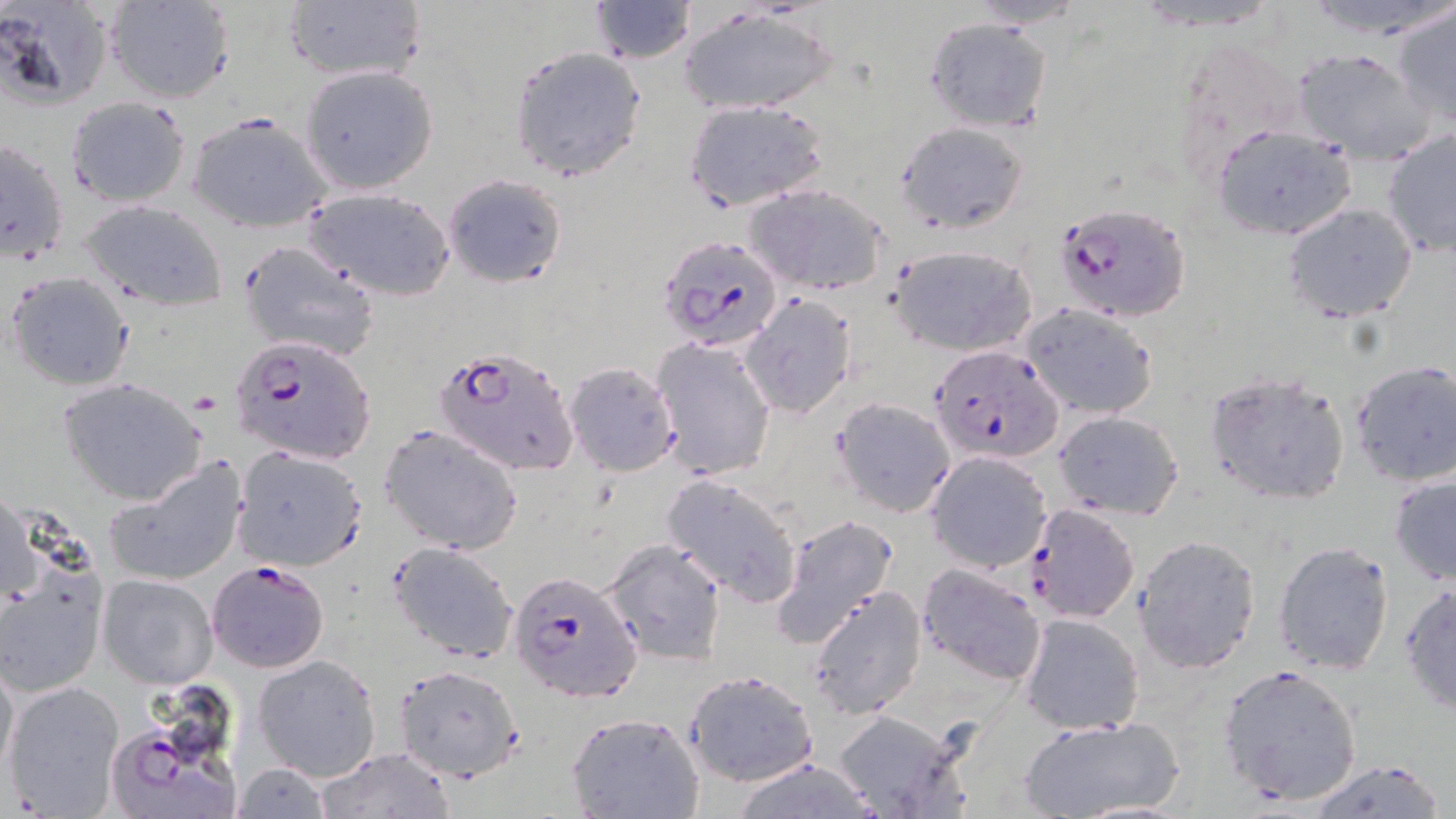
Approximate bounding boxes as named x1/y1/x2/y2 corners in pixels. Platelet locations: (x1=190, y1=391, x2=221, y2=416). Plasmodium falciparum-infected red blood cell locations: (x1=1053, y1=201, x2=1191, y2=322), (x1=656, y1=233, x2=786, y2=351), (x1=232, y1=335, x2=376, y2=463), (x1=431, y1=344, x2=578, y2=478), (x1=931, y1=344, x2=1064, y2=463), (x1=1025, y1=503, x2=1140, y2=623), (x1=206, y1=560, x2=329, y2=674), (x1=507, y1=570, x2=644, y2=701), (x1=110, y1=716, x2=247, y2=819). Uninfected red blood cell locations: (x1=1, y1=0, x2=115, y2=111), (x1=104, y1=0, x2=235, y2=104), (x1=283, y1=0, x2=429, y2=85), (x1=970, y1=0, x2=1087, y2=28), (x1=1298, y1=0, x2=1455, y2=36), (x1=588, y1=1, x2=697, y2=63), (x1=1390, y1=3, x2=1455, y2=130), (x1=679, y1=9, x2=838, y2=115), (x1=923, y1=16, x2=1052, y2=134), (x1=508, y1=44, x2=649, y2=182), (x1=1290, y1=47, x2=1435, y2=162), (x1=300, y1=65, x2=439, y2=195), (x1=65, y1=97, x2=191, y2=206), (x1=683, y1=99, x2=831, y2=213), (x1=189, y1=114, x2=329, y2=233), (x1=895, y1=121, x2=1029, y2=235), (x1=1210, y1=123, x2=1358, y2=241), (x1=1382, y1=132, x2=1455, y2=257), (x1=0, y1=137, x2=70, y2=264), (x1=441, y1=174, x2=568, y2=287), (x1=743, y1=183, x2=891, y2=297), (x1=304, y1=188, x2=456, y2=301), (x1=81, y1=199, x2=227, y2=310), (x1=1282, y1=202, x2=1418, y2=323), (x1=237, y1=240, x2=379, y2=362), (x1=885, y1=244, x2=1038, y2=355), (x1=5, y1=271, x2=133, y2=391), (x1=740, y1=295, x2=857, y2=419), (x1=1020, y1=301, x2=1161, y2=419), (x1=651, y1=337, x2=777, y2=480), (x1=1349, y1=358, x2=1456, y2=487), (x1=562, y1=361, x2=681, y2=476), (x1=1204, y1=371, x2=1352, y2=505), (x1=59, y1=377, x2=207, y2=506), (x1=831, y1=397, x2=956, y2=518), (x1=1051, y1=410, x2=1184, y2=521), (x1=378, y1=423, x2=524, y2=556), (x1=232, y1=444, x2=368, y2=572), (x1=925, y1=451, x2=1052, y2=573), (x1=102, y1=458, x2=248, y2=587), (x1=1388, y1=472, x2=1456, y2=587), (x1=661, y1=474, x2=802, y2=607), (x1=1, y1=491, x2=38, y2=608), (x1=769, y1=515, x2=899, y2=650), (x1=1131, y1=534, x2=1262, y2=673), (x1=601, y1=537, x2=727, y2=667), (x1=387, y1=540, x2=519, y2=664), (x1=1272, y1=543, x2=1396, y2=675), (x1=0, y1=557, x2=107, y2=698), (x1=915, y1=561, x2=1047, y2=686), (x1=97, y1=573, x2=220, y2=691), (x1=1398, y1=583, x2=1455, y2=713), (x1=806, y1=585, x2=927, y2=719), (x1=1018, y1=612, x2=1145, y2=735), (x1=252, y1=653, x2=382, y2=780), (x1=0, y1=655, x2=18, y2=787), (x1=1216, y1=663, x2=1363, y2=807), (x1=394, y1=664, x2=524, y2=783), (x1=683, y1=669, x2=819, y2=787), (x1=4, y1=680, x2=126, y2=816), (x1=826, y1=708, x2=972, y2=819), (x1=566, y1=712, x2=703, y2=819), (x1=1014, y1=714, x2=1190, y2=819), (x1=316, y1=747, x2=455, y2=819), (x1=1303, y1=758, x2=1450, y2=818), (x1=725, y1=759, x2=887, y2=818), (x1=231, y1=763, x2=330, y2=819). Slide-level diagnosis: Plasmodium falciparum. One field of a larger specimen. Thin blood smear. Optical microscopy. Image is 1456×819 pixels. May-Grünwald-Giemsa-stained preparation. 1000x magnification.